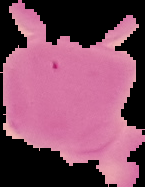 From a thin blood smear. Image is 145×187 pixels. Cell region segmented out of the field of view; the surrounding area is masked to black. Malaria status: uninfected.